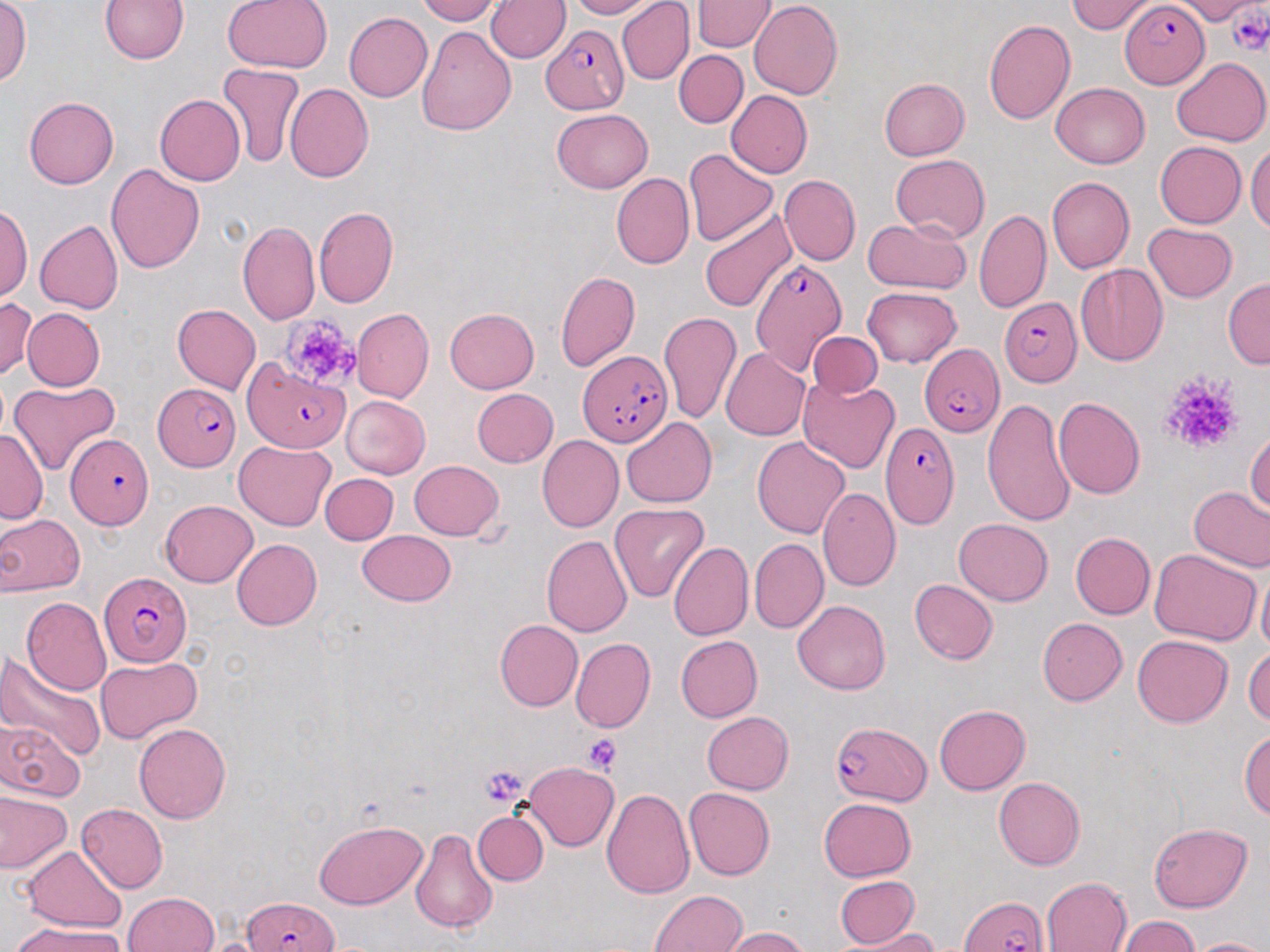

Summary:
  - Coordinate format: approximate bounding boxes as [x1, y1, x2, y2] in pixels
  - Plasmodium falciparum-infected red blood cell locations: [1119, 2, 1210, 87], [540, 25, 629, 114], [750, 259, 848, 374], [999, 298, 1081, 388], [914, 337, 1001, 441], [579, 350, 671, 448], [240, 358, 350, 453], [153, 383, 241, 471], [878, 420, 959, 532], [68, 433, 152, 529], [98, 574, 195, 665], [830, 720, 932, 804], [959, 893, 1051, 952], [240, 896, 343, 952]
  - Uninfected red blood cell locations: [1, 0, 31, 93], [99, 0, 190, 66], [223, 0, 331, 73], [412, 0, 498, 24], [562, 0, 660, 19], [618, 0, 694, 84], [1069, 0, 1152, 34], [1180, 0, 1250, 25], [486, 1, 570, 64], [693, 1, 773, 52], [748, 2, 844, 101], [342, 12, 432, 103], [984, 17, 1076, 127], [416, 22, 516, 134], [673, 50, 746, 128], [1170, 56, 1270, 146], [217, 64, 304, 170], [879, 78, 970, 162], [1051, 83, 1151, 168], [284, 84, 374, 182], [724, 90, 813, 179], [153, 93, 244, 186], [24, 96, 118, 188], [549, 109, 653, 193], [1247, 138, 1270, 242], [1153, 141, 1247, 228], [685, 150, 777, 244], [891, 155, 987, 242], [105, 163, 204, 276], [612, 172, 694, 269], [778, 175, 859, 267], [1047, 178, 1134, 273], [0, 204, 31, 304], [700, 205, 797, 310], [314, 207, 399, 307], [974, 207, 1052, 314], [861, 216, 972, 296], [34, 219, 124, 314], [238, 220, 321, 324], [1143, 222, 1240, 302], [1073, 264, 1169, 367], [554, 269, 642, 371], [1224, 278, 1269, 370], [863, 288, 961, 365], [0, 297, 38, 379], [169, 303, 259, 393], [20, 307, 106, 391], [352, 308, 434, 401], [445, 308, 540, 393], [659, 311, 741, 423], [810, 331, 884, 398], [721, 346, 810, 441], [799, 378, 900, 474], [8, 379, 122, 473], [471, 387, 558, 468], [341, 396, 430, 478], [1054, 396, 1147, 498], [980, 399, 1075, 524], [620, 417, 718, 508], [0, 427, 46, 523], [1247, 431, 1270, 524], [536, 435, 623, 532], [752, 436, 851, 540], [234, 439, 335, 530], [408, 458, 504, 538], [319, 473, 397, 546], [1187, 486, 1270, 572], [818, 487, 899, 592], [159, 501, 258, 586], [610, 502, 708, 601], [0, 512, 83, 596], [954, 518, 1054, 605], [357, 529, 457, 607], [1071, 533, 1154, 619], [541, 535, 631, 636], [751, 538, 827, 633], [232, 539, 322, 630], [667, 542, 751, 642], [1147, 549, 1260, 645], [1254, 572, 1269, 661], [910, 579, 997, 664], [24, 597, 112, 696], [792, 598, 891, 694], [1037, 617, 1127, 706], [494, 618, 581, 712], [1132, 632, 1232, 724], [675, 635, 762, 723], [569, 639, 653, 733], [1245, 642, 1269, 730], [0, 651, 104, 760], [95, 655, 202, 742], [934, 704, 1032, 793], [703, 710, 796, 794], [2, 718, 84, 801], [134, 723, 231, 824], [1241, 727, 1270, 822], [520, 761, 619, 849], [993, 775, 1085, 867], [602, 786, 694, 897], [685, 787, 778, 880], [1, 794, 72, 875], [817, 798, 915, 881], [75, 804, 168, 893], [475, 811, 547, 887], [313, 819, 429, 907], [1146, 822, 1252, 911], [409, 825, 499, 937], [21, 846, 126, 932], [833, 875, 922, 948], [1040, 876, 1132, 952], [648, 889, 752, 952], [122, 891, 219, 952], [1119, 916, 1201, 952], [12, 921, 126, 952], [722, 925, 813, 951], [862, 929, 945, 951], [1191, 935, 1270, 952]
  - Platelet locations: [1228, 4, 1270, 53], [284, 316, 361, 388], [1158, 368, 1247, 457], [584, 735, 622, 772], [479, 763, 527, 807]
  - Slide-level diagnosis: Plasmodium falciparum
  - Field of view: one of a larger specimen
  - Stain: May-Grünwald-Giemsa
  - Magnification: 1000x
  - Preparation: thin blood film
  - Image size: 1270×952 pixels
  - Modality: optical microscopy